Give the extent of all uninfected red blood cells.
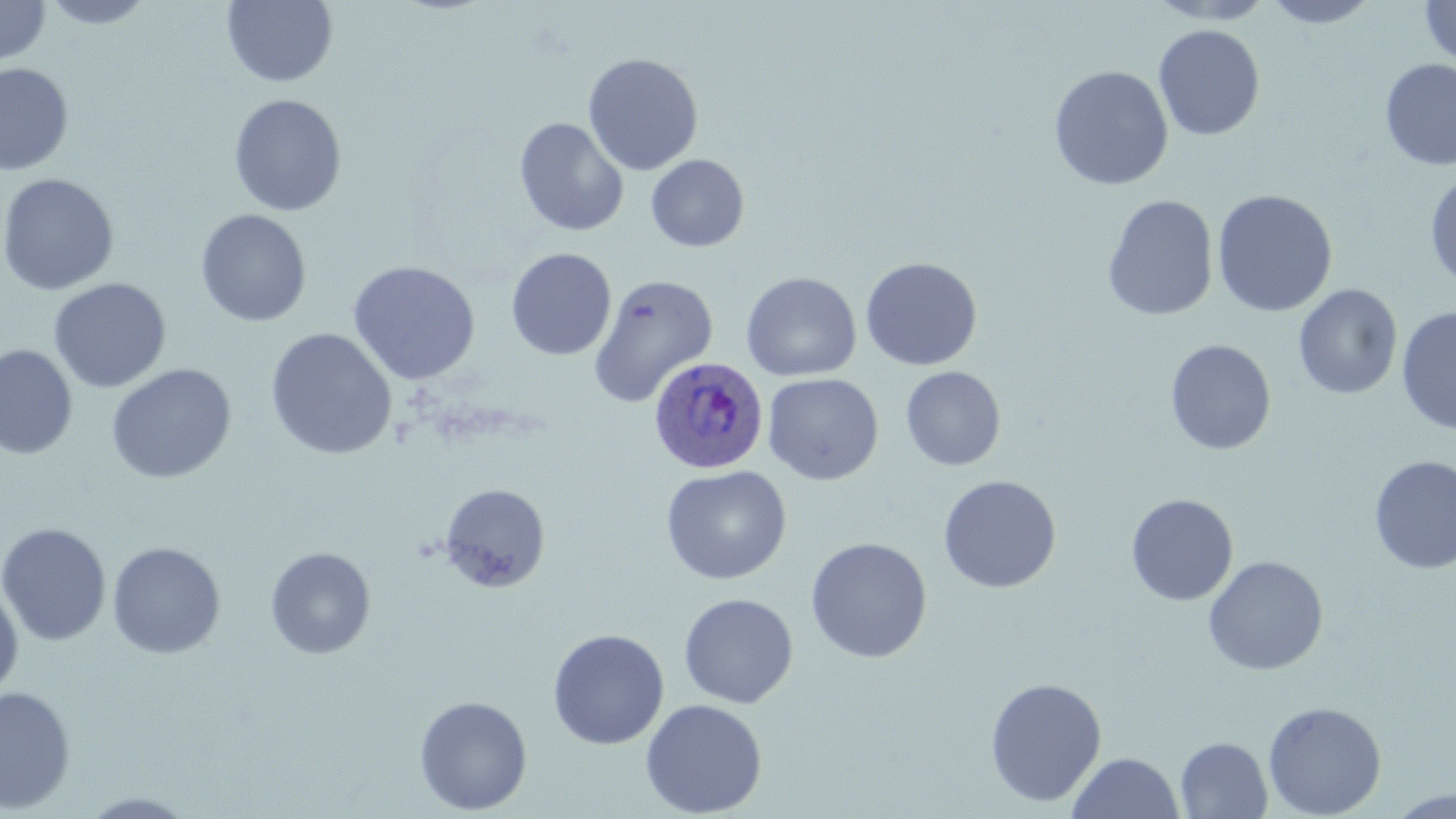

Approximate bounding boxes as (x1, y1, x2, y2) in pixels.
Uninfected red blood cells: (39, 0, 156, 29), (1260, 0, 1382, 29), (1420, 0, 1455, 69), (0, 1, 51, 66), (222, 1, 338, 88), (1153, 24, 1266, 141), (582, 52, 704, 176), (1379, 59, 1456, 171), (0, 63, 75, 177), (1048, 65, 1174, 191), (228, 93, 347, 217), (514, 117, 629, 237), (646, 154, 750, 253), (1425, 171, 1456, 292), (0, 173, 120, 296), (1212, 189, 1338, 318), (1102, 194, 1219, 321), (194, 209, 312, 327), (505, 248, 617, 361), (860, 257, 983, 371), (347, 260, 481, 385), (740, 271, 861, 381), (587, 274, 720, 408), (49, 278, 171, 393), (1293, 283, 1403, 400), (1396, 307, 1456, 435), (264, 328, 397, 461), (1165, 338, 1277, 455), (0, 343, 78, 460), (105, 363, 237, 484), (901, 366, 1006, 471), (763, 373, 884, 486), (1369, 455, 1456, 574), (660, 465, 792, 585), (938, 475, 1061, 594), (439, 483, 551, 593), (1125, 493, 1239, 606), (0, 522, 112, 646), (805, 537, 932, 663), (107, 541, 227, 659), (265, 546, 376, 659), (1203, 555, 1329, 676), (0, 580, 24, 701), (678, 593, 799, 709), (547, 628, 669, 750), (984, 677, 1107, 807), (1, 686, 76, 814), (414, 694, 532, 815), (640, 698, 768, 817), (1262, 700, 1387, 818), (1175, 737, 1272, 819), (1066, 751, 1184, 818), (1387, 789, 1455, 819), (77, 791, 202, 817).

Summary:
  - Plasmodium ovale-infected red blood cell locations: (649, 356, 769, 474)
  - Slide-level diagnosis: Plasmodium ovale
  - Field of view: single
  - Magnification: 1000x
  - Stain: May-Grünwald-Giemsa
  - Preparation: thin blood smear
  - Modality: light microscopy
  - Image size: 1456×819 pixels